State the blood parasite species.
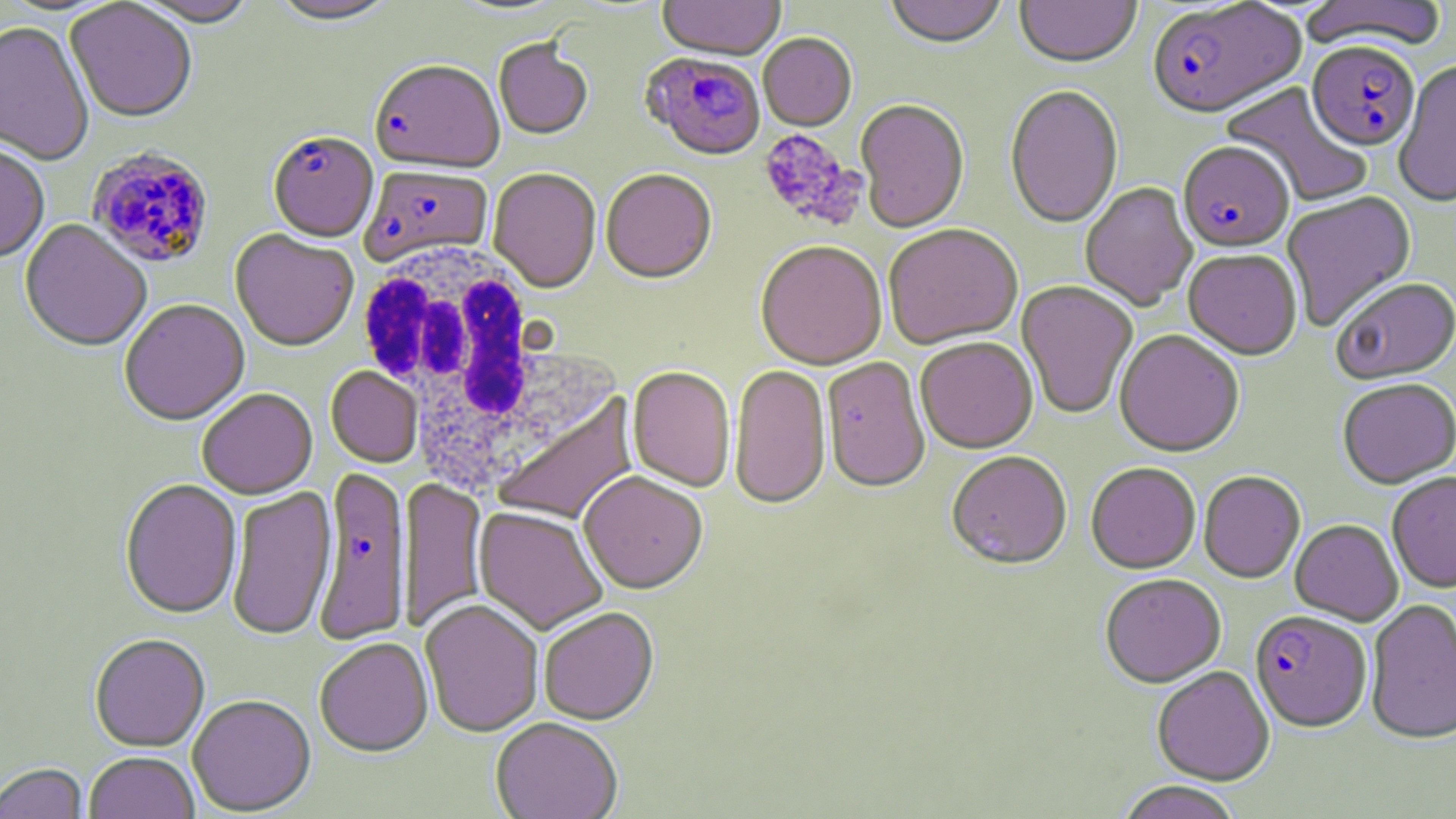

Plasmodium falciparum.

magnification = 1000x
Plasmodium falciparum-infected red blood cell locations = approximate bounding boxes as (x1,y1)-(x2,y2) corner pairs in pixels: (1147,2)-(1305,122), (1306,44)-(1420,154), (641,55)-(766,163), (370,63)-(505,176), (268,135)-(378,245), (1178,144)-(1294,255), (86,147)-(215,271), (359,167)-(492,269), (314,472)-(412,647), (1250,612)-(1371,733)
image size = 1456×819 pixels
preparation = thin blood smear
uninfected red blood cell locations = approximate bounding boxes as (x1,y1)-(x2,y2) corner pairs in pixels: (128,0)-(259,30), (267,0)-(400,29), (450,0)-(569,17), (657,0)-(786,63), (884,0)-(1008,51), (1015,0)-(1141,71), (1299,0)-(1449,53), (65,2)-(197,125), (0,23)-(94,167), (758,35)-(857,132), (493,42)-(593,142), (1393,62)-(1456,210), (1221,82)-(1372,208), (1005,86)-(1123,231), (855,100)-(970,236), (0,146)-(50,266), (487,169)-(601,295), (601,171)-(717,286), (1080,183)-(1198,312), (1281,192)-(1417,332), (20,220)-(151,355), (884,226)-(1023,351), (229,230)-(359,354), (755,243)-(887,372), (1183,251)-(1302,362), (1333,280)-(1456,386), (1016,281)-(1138,420), (119,301)-(250,428), (1114,331)-(1244,459), (916,339)-(1039,455), (822,359)-(930,496), (729,366)-(831,511), (325,367)-(423,469), (627,368)-(735,493), (1338,380)-(1456,491), (197,389)-(318,501), (493,392)-(640,527), (947,454)-(1073,572), (1086,463)-(1201,575), (1198,472)-(1305,584), (578,473)-(708,597), (1387,473)-(1456,593), (399,479)-(488,633), (120,481)-(242,621), (226,486)-(338,642), (472,508)-(609,636), (1290,520)-(1403,626), (1100,575)-(1226,688), (1365,599)-(1456,745), (420,601)-(543,738), (539,609)-(659,727), (89,636)-(210,753), (314,640)-(433,760), (1152,668)-(1274,785), (188,697)-(316,816), (490,720)-(623,819), (84,753)-(200,819), (1,764)-(89,819), (1115,782)-(1243,819)
platelet locations = approximate bounding boxes as (x1,y1)-(x2,y2) corner pairs in pixels: (758,130)-(864,230)
stain = May-Grünwald-Giemsa
modality = light microscopy
field of view = one of a larger specimen
white blood cell locations = approximate bounding boxes as (x1,y1)-(x2,y2) corner pairs in pixels: (354,241)-(583,489)